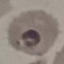
Result: malaria parasites identified. Giemsa stain. Automatically extracted cell patch, resized to 64 × 64 pixels. Thin blood film. Photographed with a smartphone camera at the microscope eyepiece.